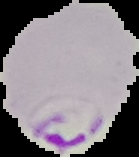
preparation = thin blood film
image size = 139×157 pixels
image type = segmented cell region with the area outside set to black
malaria status = parasitized